Identify the blood parasite species.
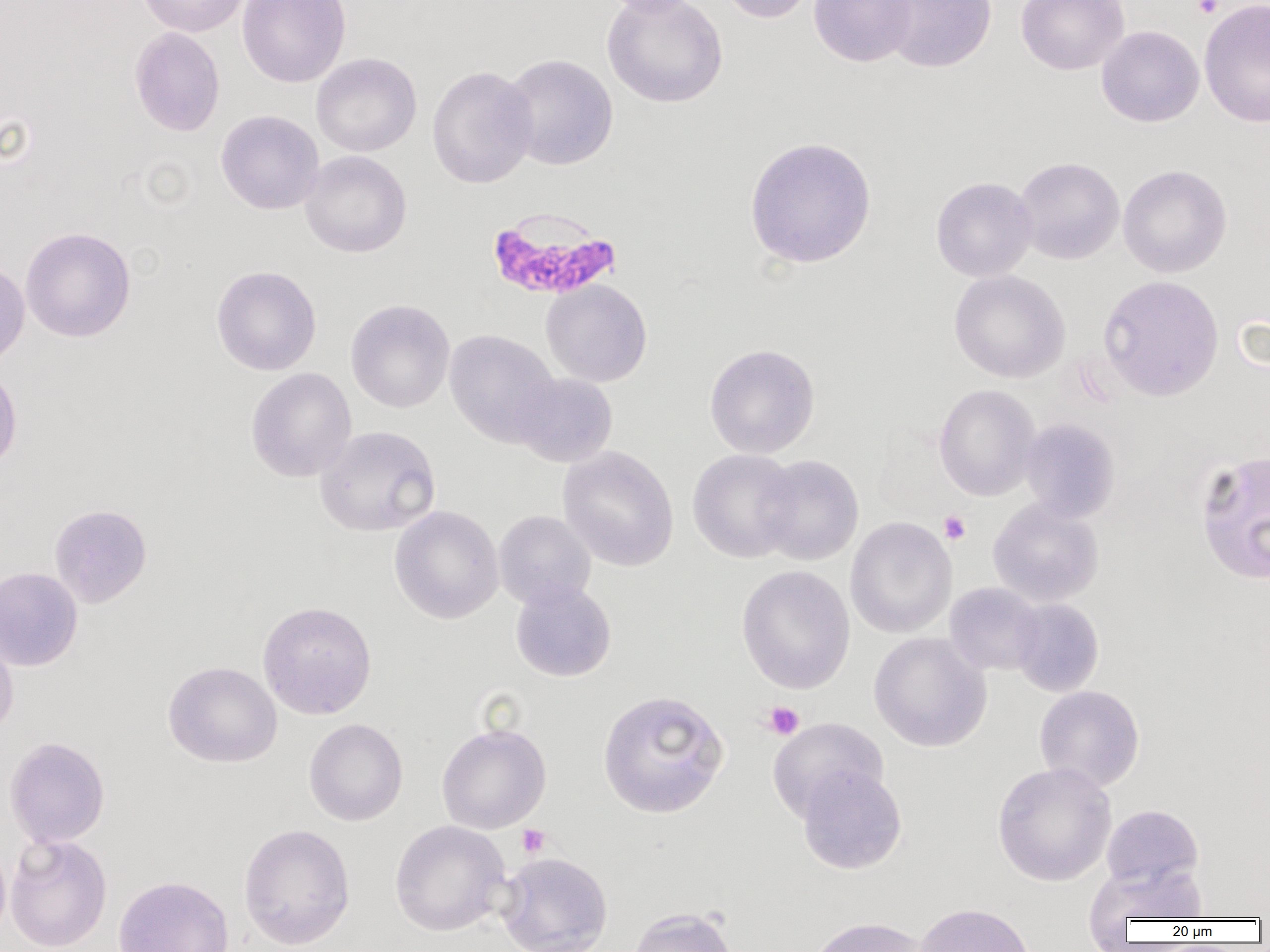
Plasmodium falciparum.

Approximate bounding boxes as [x1, y1, x2, y2] in pixels. Plasmodium falciparum-infected red blood cell locations: [486, 209, 623, 302]. Platelet locations: [1192, 0, 1223, 18], [939, 511, 971, 544], [761, 701, 805, 740], [516, 824, 550, 858]. Uninfected red blood cell locations: [136, 0, 249, 37], [237, 0, 351, 88], [596, 0, 708, 18], [601, 0, 729, 108], [717, 0, 818, 23], [808, 0, 917, 67], [879, 0, 997, 73], [1015, 0, 1130, 75], [1199, 0, 1270, 128], [1096, 25, 1204, 127], [129, 27, 225, 137], [311, 52, 422, 157], [501, 53, 619, 171], [427, 65, 538, 189], [215, 110, 324, 215], [743, 136, 877, 269], [300, 151, 412, 258], [1014, 156, 1125, 264], [1118, 164, 1232, 278], [931, 176, 1038, 282], [20, 227, 136, 342], [0, 258, 30, 370], [211, 265, 322, 375], [949, 269, 1070, 383], [1098, 275, 1224, 402], [541, 279, 652, 387], [345, 300, 455, 413], [444, 329, 562, 447], [704, 343, 821, 458], [0, 365, 22, 474], [246, 367, 357, 482], [511, 373, 618, 467], [934, 384, 1040, 501], [1020, 418, 1121, 523], [315, 425, 441, 537], [558, 446, 679, 572], [688, 448, 801, 563], [1194, 450, 1270, 585], [754, 454, 865, 566], [988, 498, 1103, 607], [49, 503, 152, 608], [389, 506, 504, 624], [493, 510, 596, 609], [845, 516, 957, 638], [736, 565, 855, 694], [0, 566, 83, 671], [510, 580, 616, 682], [945, 582, 1045, 676], [1010, 598, 1104, 697], [257, 600, 377, 720], [0, 625, 19, 740], [869, 632, 992, 752], [163, 661, 282, 767], [1034, 685, 1145, 792], [597, 690, 730, 819], [767, 716, 889, 822], [304, 718, 408, 826], [436, 722, 551, 834], [4, 736, 110, 847], [992, 761, 1117, 886], [797, 765, 907, 874], [1101, 804, 1204, 890], [389, 820, 511, 937], [238, 823, 356, 950], [4, 833, 112, 952], [0, 839, 11, 944], [495, 851, 613, 952], [1086, 862, 1208, 929], [113, 874, 234, 952], [913, 902, 1035, 952], [625, 906, 740, 952], [806, 916, 930, 952]. Image is 1270×952 pixels. Light microscopy. Thin blood film. Captured at 1000x magnification. One field of a larger specimen.